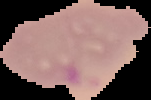

Summary:
  - Preparation: thin blood smear
  - Malaria status: parasitized
  - Image size: 151×100 pixels
  - Image type: segmented cell region with the area outside set to black